Point out each leukocyte.
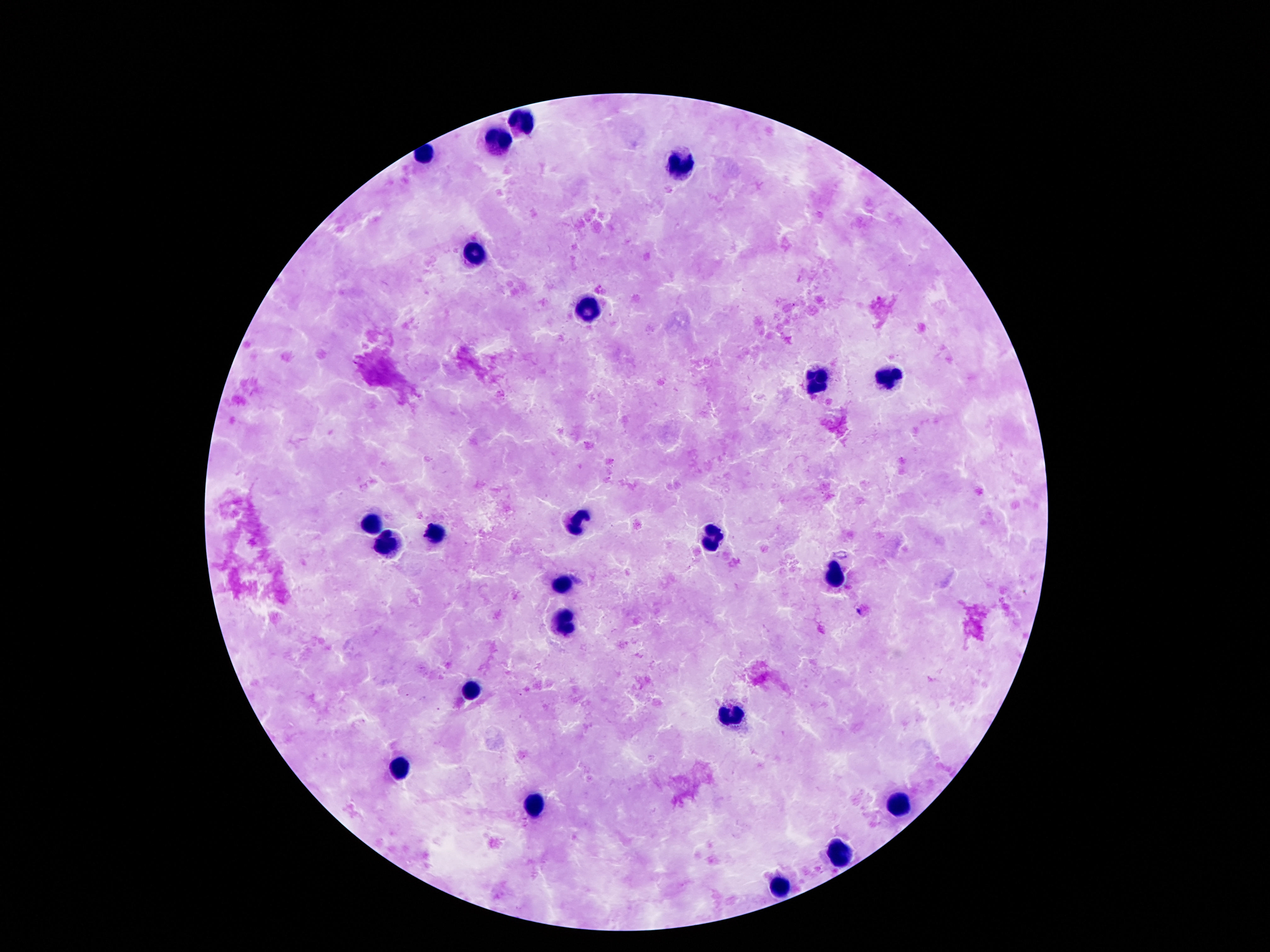
Approximate object centers, in pixels from the top-left corner.
Leukocytes: (x=521, y=122), (x=498, y=143), (x=424, y=152), (x=682, y=165), (x=472, y=254), (x=584, y=311), (x=814, y=379), (x=894, y=379), (x=581, y=519), (x=376, y=525), (x=435, y=534), (x=709, y=540), (x=390, y=546), (x=836, y=576), (x=563, y=586), (x=563, y=623), (x=472, y=688), (x=730, y=716), (x=403, y=765), (x=901, y=806), (x=533, y=810), (x=840, y=853), (x=779, y=888).

100x magnification. One field from this slide. Photographed through the microscope eyepiece with a smartphone camera. Thick blood smear. Patient malaria status: not infected. Image is 1270×952 pixels. Giemsa-stained preparation.